Assess this cell for malaria.
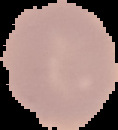
Uninfected.

image type = segmented cell region with the area outside set to black
image size = 118×130 pixels
preparation = thin blood smear